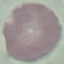

Summary:
  - Result: no malaria parasites seen
  - Stain: Giemsa
  - Preparation: thin blood film
  - Capture: smartphone camera at the microscope eyepiece
  - Image type: automatically extracted cell patch, resized to 64 × 64 pixels